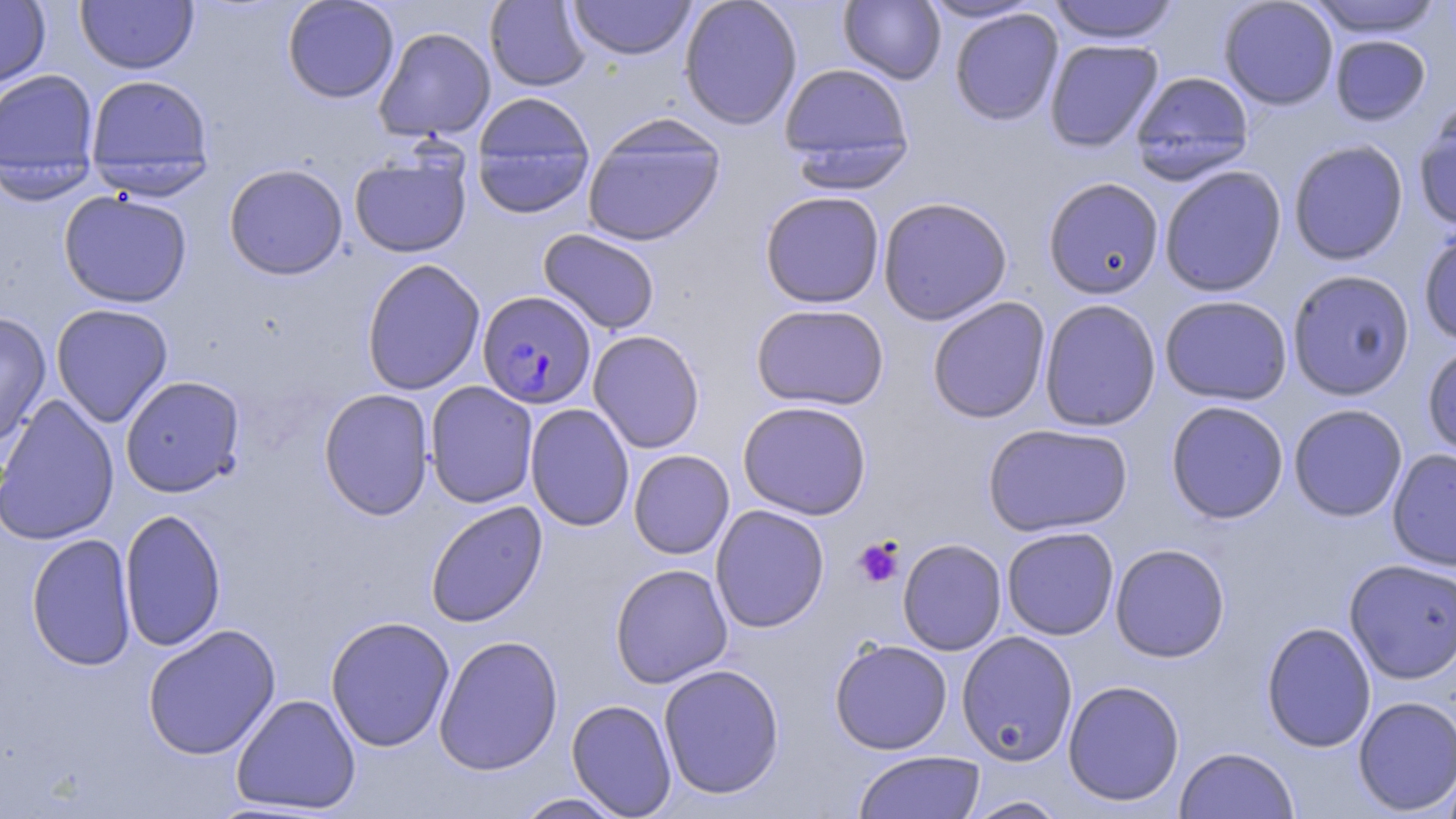

slide-level diagnosis = Plasmodium falciparum
image size = 1456×819 pixels
Plasmodium falciparum-infected red blood cell locations = approximate bounding boxes as (x1, y1, x2, y2) in pixels: (477, 290, 596, 409)
preparation = thin blood film
platelet locations = approximate bounding boxes as (x1, y1, x2, y2) in pixels: (853, 538, 903, 588)
field of view = one of a larger specimen
uninfected red blood cell locations = approximate bounding boxes as (x1, y1, x2, y2) in pixels: (0, 0, 51, 89), (76, 0, 199, 74), (282, 0, 399, 103), (567, 0, 696, 60), (679, 0, 802, 130), (838, 0, 946, 84), (919, 0, 1044, 23), (1048, 0, 1181, 44), (1218, 0, 1339, 110), (485, 1, 592, 91), (1302, 1, 1446, 38), (950, 8, 1064, 126), (373, 26, 496, 143), (1329, 35, 1431, 125), (1044, 39, 1164, 153), (778, 61, 914, 182), (0, 69, 100, 172), (1129, 71, 1255, 184), (83, 74, 215, 185), (472, 95, 595, 216), (1414, 99, 1456, 232), (581, 119, 726, 248), (1288, 139, 1409, 265), (349, 152, 472, 258), (2, 163, 101, 205), (223, 163, 349, 280), (1159, 166, 1286, 297), (1042, 177, 1165, 299), (58, 190, 193, 308), (760, 191, 885, 308), (877, 196, 1012, 325), (1418, 227, 1456, 346), (538, 228, 661, 334), (361, 258, 486, 395), (1286, 268, 1415, 400), (1159, 294, 1292, 406), (927, 297, 1051, 424), (1039, 298, 1161, 432), (751, 302, 890, 411), (51, 303, 174, 427), (0, 311, 52, 450), (587, 330, 705, 453), (1422, 341, 1456, 462), (120, 375, 245, 497), (424, 380, 539, 509), (318, 388, 435, 520), (0, 394, 119, 546), (737, 400, 872, 520), (1165, 400, 1289, 524), (525, 403, 635, 532), (1288, 404, 1408, 522), (983, 423, 1133, 537), (1387, 447, 1456, 571), (628, 449, 734, 559), (425, 500, 548, 627), (710, 504, 830, 633), (119, 507, 226, 652), (1001, 526, 1119, 640), (26, 533, 137, 671), (897, 538, 1007, 656), (1109, 543, 1230, 662), (1344, 559, 1456, 684), (609, 563, 733, 688), (325, 615, 455, 752), (1261, 621, 1377, 753), (142, 623, 281, 760), (956, 631, 1078, 766), (434, 634, 563, 776), (829, 638, 952, 755), (658, 663, 785, 799), (1062, 680, 1185, 806), (231, 693, 361, 814), (1352, 696, 1456, 815), (566, 699, 677, 818), (1174, 746, 1299, 819), (854, 750, 986, 818), (1438, 759, 1456, 819), (511, 792, 631, 818), (961, 795, 1071, 818)
stain = May-Grünwald-Giemsa
modality = optical microscopy
magnification = 1000x